State the blood parasite species.
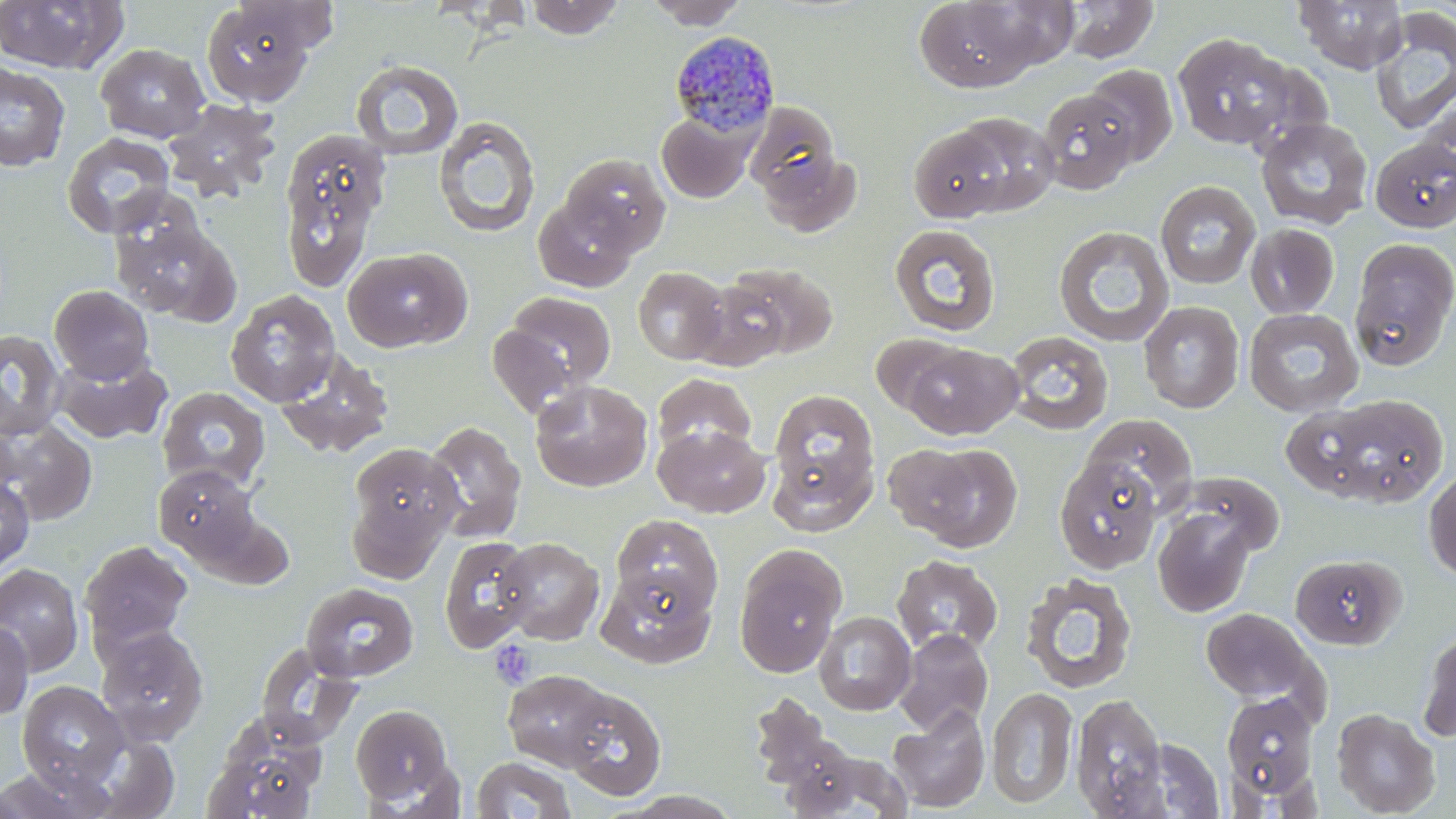
Plasmodium malariae.

Approximate bounding boxes as named x1/y1/x2/y2 corners in pixels. Uninfected red blood cell locations: (x1=0, y1=0, x2=129, y2=75), (x1=525, y1=0, x2=626, y2=39), (x1=644, y1=0, x2=748, y2=29), (x1=913, y1=0, x2=1046, y2=92), (x1=1061, y1=0, x2=1159, y2=63), (x1=1293, y1=0, x2=1408, y2=74), (x1=234, y1=1, x2=341, y2=52), (x1=200, y1=2, x2=317, y2=107), (x1=1370, y1=8, x2=1456, y2=136), (x1=1172, y1=32, x2=1296, y2=151), (x1=94, y1=43, x2=210, y2=143), (x1=1229, y1=55, x2=1336, y2=159), (x1=351, y1=59, x2=464, y2=160), (x1=0, y1=61, x2=70, y2=172), (x1=1082, y1=64, x2=1178, y2=168), (x1=1036, y1=88, x2=1141, y2=194), (x1=1418, y1=95, x2=1456, y2=187), (x1=163, y1=99, x2=281, y2=201), (x1=746, y1=107, x2=857, y2=232), (x1=657, y1=112, x2=754, y2=202), (x1=949, y1=112, x2=1061, y2=216), (x1=433, y1=116, x2=540, y2=238), (x1=1255, y1=117, x2=1374, y2=230), (x1=907, y1=124, x2=1010, y2=223), (x1=277, y1=128, x2=390, y2=289), (x1=61, y1=132, x2=176, y2=238), (x1=1371, y1=138, x2=1456, y2=233), (x1=559, y1=152, x2=671, y2=259), (x1=1155, y1=180, x2=1261, y2=290), (x1=533, y1=193, x2=641, y2=292), (x1=111, y1=213, x2=241, y2=324), (x1=889, y1=224, x2=1001, y2=336), (x1=1053, y1=224, x2=1174, y2=347), (x1=1245, y1=224, x2=1340, y2=319), (x1=1350, y1=240, x2=1456, y2=369), (x1=343, y1=246, x2=472, y2=352), (x1=723, y1=262, x2=839, y2=360), (x1=633, y1=267, x2=729, y2=365), (x1=690, y1=279, x2=792, y2=371), (x1=49, y1=285, x2=155, y2=385), (x1=226, y1=290, x2=340, y2=407), (x1=499, y1=291, x2=617, y2=398), (x1=1138, y1=301, x2=1244, y2=413), (x1=1243, y1=308, x2=1364, y2=417), (x1=0, y1=329, x2=67, y2=441), (x1=1003, y1=330, x2=1114, y2=436), (x1=870, y1=333, x2=968, y2=416), (x1=901, y1=343, x2=1021, y2=439), (x1=274, y1=348, x2=394, y2=458), (x1=53, y1=352, x2=172, y2=444), (x1=652, y1=371, x2=757, y2=458), (x1=530, y1=379, x2=653, y2=492), (x1=157, y1=387, x2=270, y2=493), (x1=765, y1=387, x2=882, y2=530), (x1=1323, y1=394, x2=1449, y2=507), (x1=1281, y1=404, x2=1383, y2=500), (x1=1082, y1=412, x2=1198, y2=514), (x1=0, y1=418, x2=97, y2=526), (x1=423, y1=420, x2=527, y2=543), (x1=654, y1=423, x2=770, y2=518), (x1=346, y1=440, x2=462, y2=574), (x1=882, y1=442, x2=983, y2=538), (x1=914, y1=443, x2=1022, y2=549), (x1=1054, y1=456, x2=1163, y2=574), (x1=153, y1=464, x2=261, y2=563), (x1=1423, y1=468, x2=1456, y2=582), (x1=1176, y1=472, x2=1282, y2=559), (x1=0, y1=474, x2=35, y2=573), (x1=1152, y1=506, x2=1256, y2=617), (x1=612, y1=514, x2=723, y2=617), (x1=439, y1=536, x2=538, y2=653), (x1=496, y1=537, x2=604, y2=645), (x1=80, y1=539, x2=194, y2=652), (x1=734, y1=546, x2=847, y2=677), (x1=892, y1=554, x2=1003, y2=657), (x1=0, y1=563, x2=84, y2=676), (x1=597, y1=566, x2=715, y2=668), (x1=1021, y1=572, x2=1136, y2=694), (x1=301, y1=582, x2=420, y2=682), (x1=1200, y1=607, x2=1321, y2=706), (x1=814, y1=611, x2=916, y2=715), (x1=0, y1=620, x2=33, y2=720), (x1=95, y1=625, x2=210, y2=745), (x1=1418, y1=628, x2=1456, y2=744), (x1=894, y1=629, x2=993, y2=735), (x1=256, y1=645, x2=363, y2=748), (x1=502, y1=668, x2=618, y2=770), (x1=17, y1=680, x2=129, y2=789), (x1=559, y1=684, x2=668, y2=800), (x1=987, y1=687, x2=1078, y2=810), (x1=748, y1=691, x2=850, y2=802), (x1=1221, y1=693, x2=1319, y2=805), (x1=1071, y1=694, x2=1168, y2=817), (x1=350, y1=703, x2=454, y2=806), (x1=887, y1=705, x2=990, y2=812), (x1=1331, y1=708, x2=1440, y2=817), (x1=203, y1=723, x2=327, y2=819), (x1=1137, y1=738, x2=1226, y2=816), (x1=779, y1=745, x2=911, y2=818), (x1=471, y1=755, x2=577, y2=818), (x1=0, y1=764, x2=116, y2=818). Platelet locations: (x1=489, y1=640, x2=535, y2=689). Plasmodium malariae-infected red blood cell locations: (x1=667, y1=29, x2=781, y2=139). Captured at 1000x magnification. Thin blood smear. One field of a larger specimen. Image is 1456×819 pixels. Light microscopy. May-Grünwald-Giemsa-stained preparation.